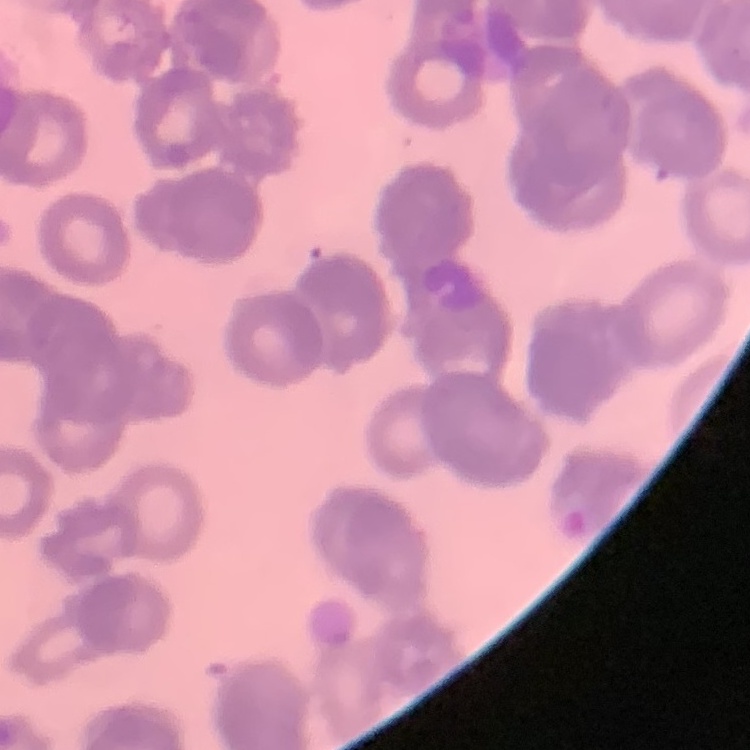

erythrocyte morphology = rouleaux formation
preparation = thin blood film
stain = Field's or Giemsa
image type = square crop of a larger photomicrograph